Point out each Plasmodium parasite.
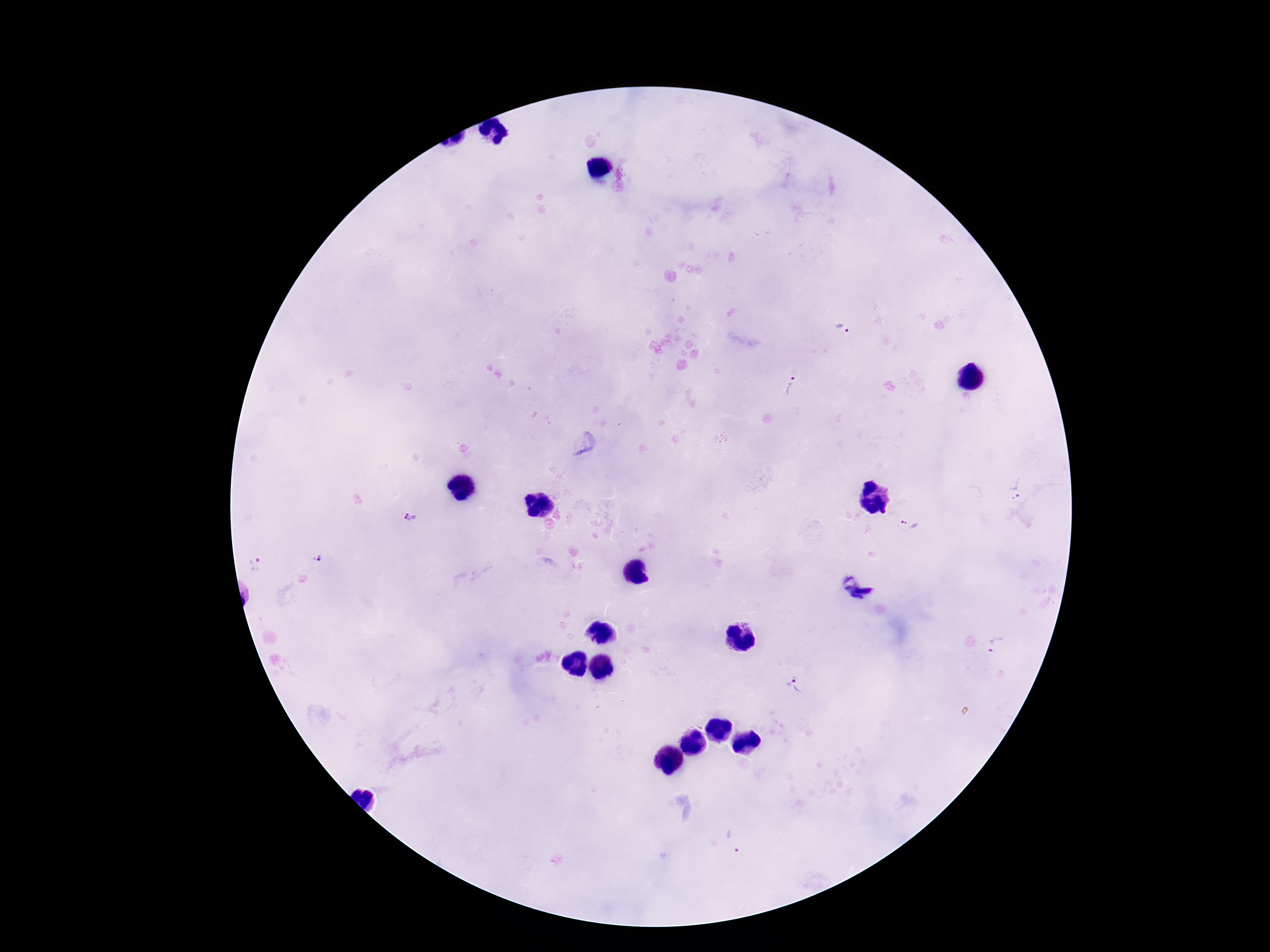
Approximate object centers, in pixels from the top-left corner.
Plasmodium parasites: (x=844, y=329), (x=790, y=386), (x=1016, y=488), (x=410, y=518), (x=909, y=524), (x=317, y=558), (x=255, y=565), (x=858, y=589), (x=998, y=646), (x=792, y=687), (x=733, y=842).

{
  "image_size": "1270×952 pixels",
  "field_of_view": "one from this slide",
  "capture": "smartphone camera through the microscope eyepiece",
  "patient_malaria_status": "positive",
  "magnification": "100x",
  "stain": "Giemsa",
  "preparation": "thick peripheral-blood smear"
}